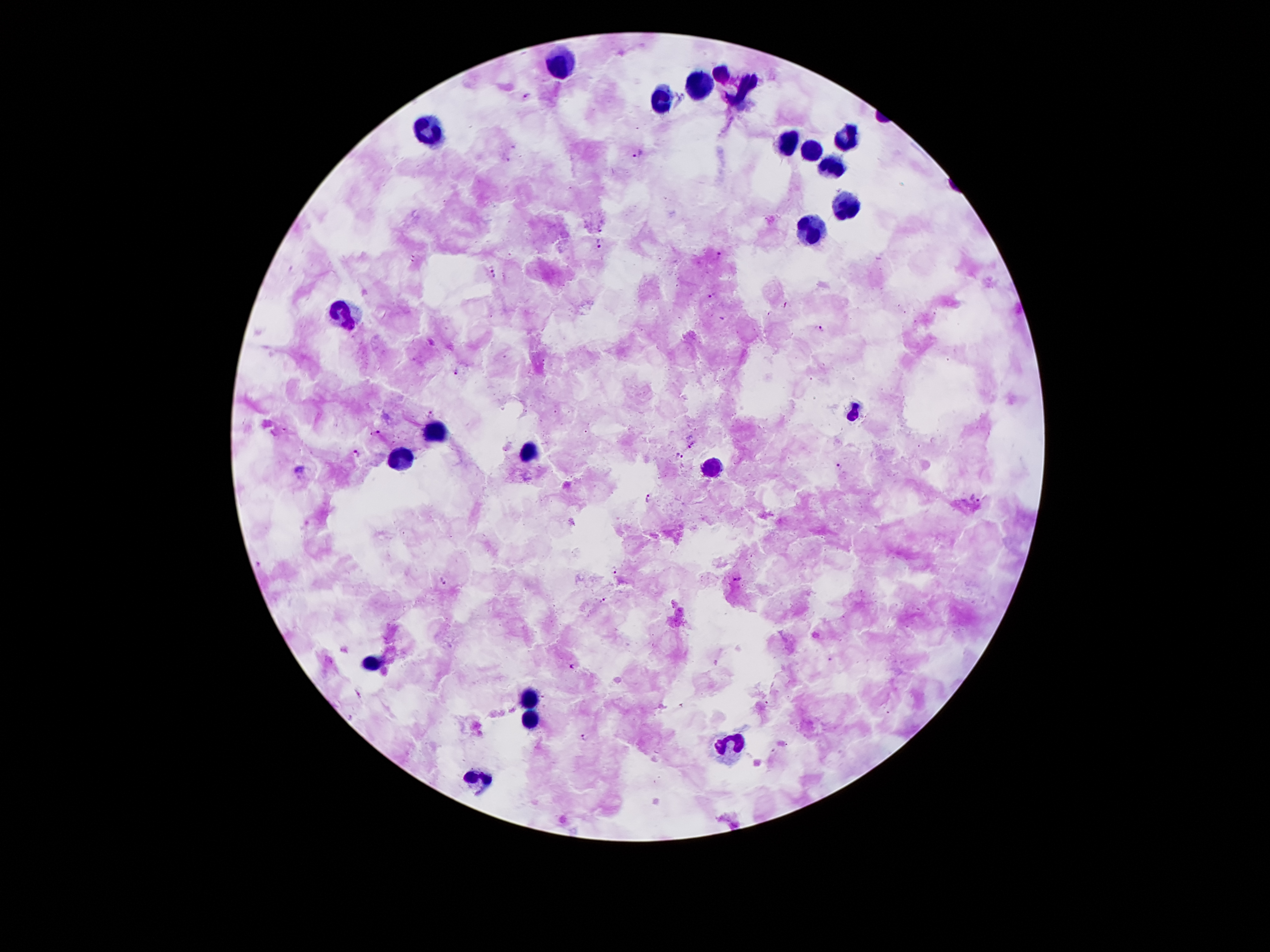

Approximate centers as (x, y) in pixels.
Summary:
  - Plasmodium parasite locations: (528, 97), (638, 153), (600, 228), (598, 243), (719, 255), (413, 258), (493, 273), (711, 295), (821, 324), (458, 370), (431, 414), (375, 434), (693, 446), (357, 453), (678, 456), (839, 467), (647, 497), (975, 497), (615, 570), (443, 580), (737, 580), (602, 599), (573, 665), (767, 702), (585, 736)
  - Leukocyte locations: (559, 65), (721, 70), (697, 85), (743, 88), (663, 98), (431, 127), (847, 135), (789, 145), (811, 149), (831, 159), (847, 205), (807, 226), (347, 314), (855, 412), (435, 426), (529, 452), (399, 460), (713, 468), (375, 664), (529, 696), (527, 720), (731, 748), (477, 782)
  - Preparation: thick peripheral-blood smear
  - Capture: smartphone through the microscope eyepiece
  - Patient malaria status: positive for Plasmodium falciparum
  - Magnification: 100x
  - Image size: 1270×952 pixels
  - Stain: Giemsa
  - Field of view: single